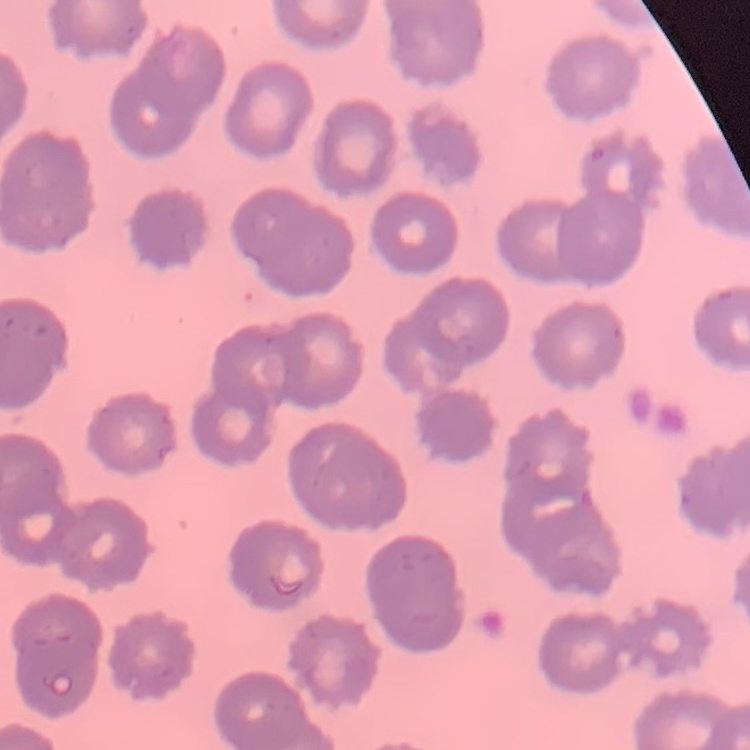

{
  "erythrocyte_morphology": "no rouleaux formation",
  "image_type": "square crop of a larger photomicrograph",
  "stain": "Field's or Giemsa",
  "preparation": "thin blood film"
}